Name the cell type shown.
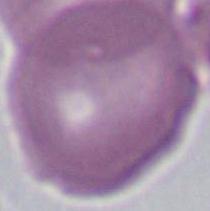
This is an erythrocyte.

modality = micrograph
magnification = 1000x